Locate every blood parasite and identify its species.
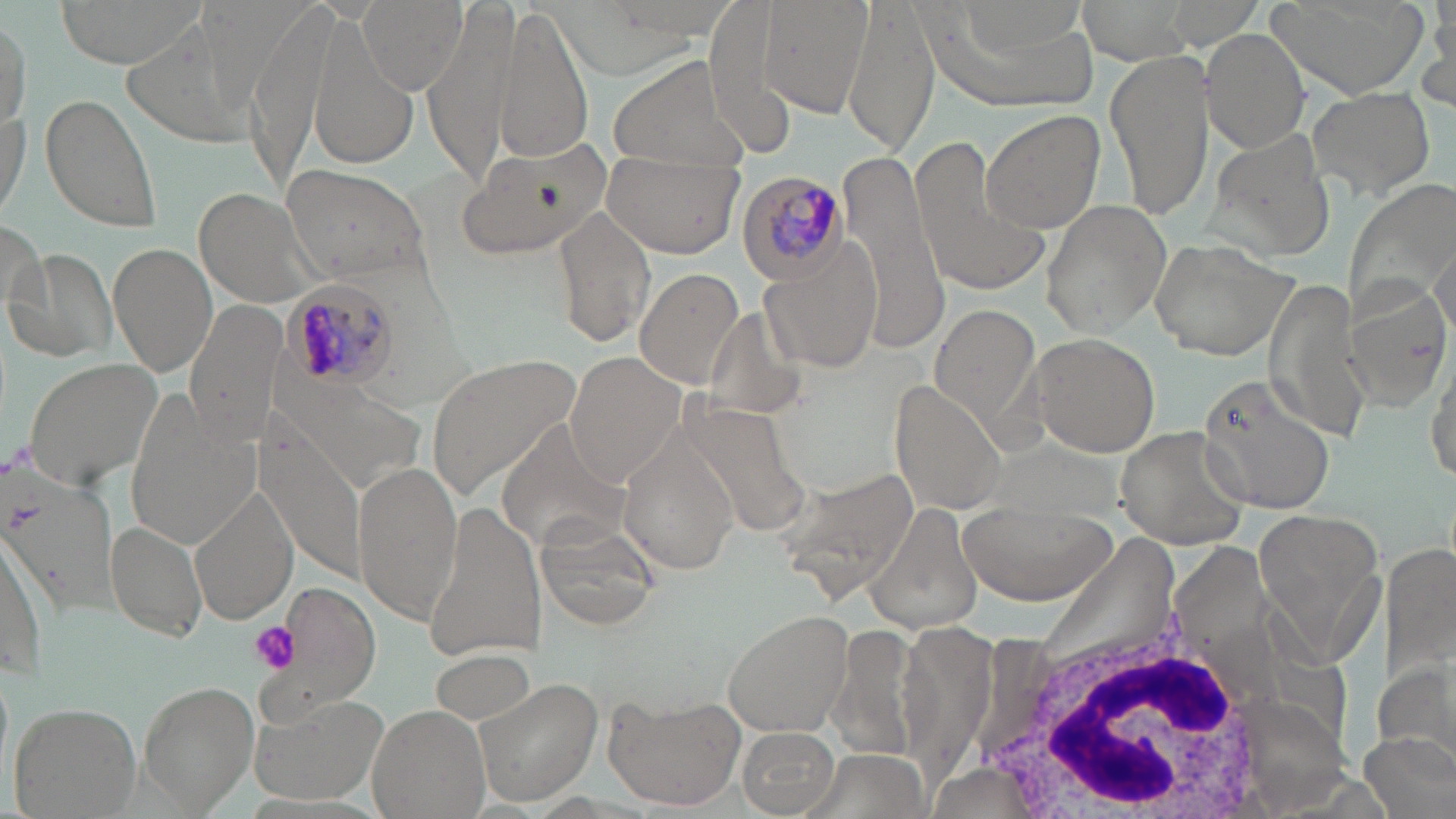

Approximate bounding boxes as [x1, y1, x2, y2] in pixels.
Plasmodium malariae-infected red blood cells: [736, 171, 849, 284], [280, 278, 398, 390].
No Plasmodium falciparum, Plasmodium ovale, Plasmodium vivax, Babesia divergens, or Trypanosoma brucei observed.

Summary:
  - Uninfected red blood cell locations: [52, 0, 205, 67], [247, 0, 341, 193], [358, 0, 465, 94], [756, 0, 874, 116], [844, 0, 938, 154], [1164, 0, 1267, 49], [1263, 0, 1429, 103], [1077, 1, 1197, 65], [425, 2, 516, 183], [1426, 3, 1455, 101], [1, 7, 31, 139], [491, 7, 594, 169], [304, 16, 418, 177], [1202, 28, 1309, 153], [1104, 50, 1215, 221], [606, 53, 750, 176], [1305, 84, 1436, 202], [41, 92, 164, 233], [0, 101, 31, 224], [979, 109, 1104, 233], [1207, 131, 1339, 261], [457, 137, 612, 262], [908, 139, 1052, 300], [841, 146, 951, 335], [600, 153, 744, 260], [278, 162, 433, 284], [1345, 177, 1456, 318], [193, 188, 327, 309], [1039, 200, 1172, 338], [549, 203, 658, 352], [1, 215, 53, 328], [1147, 238, 1298, 361], [759, 240, 884, 377], [109, 241, 217, 378], [1430, 242, 1455, 335], [5, 248, 118, 363], [633, 266, 747, 390], [1263, 281, 1376, 444], [1340, 283, 1450, 414], [183, 297, 284, 443], [928, 301, 1043, 438], [1029, 333, 1161, 458], [425, 351, 585, 498], [566, 352, 686, 482], [1426, 354, 1456, 485], [23, 357, 161, 489], [1198, 372, 1334, 517], [890, 379, 1007, 516], [128, 401, 259, 544], [496, 422, 628, 557], [1116, 423, 1251, 549], [617, 435, 742, 575], [354, 462, 465, 622], [779, 466, 920, 601], [3, 468, 117, 612], [191, 483, 299, 624], [421, 498, 546, 663], [868, 502, 985, 636], [955, 502, 1114, 607], [1254, 506, 1387, 651], [529, 516, 663, 633], [105, 518, 209, 644], [0, 535, 50, 681], [1382, 537, 1456, 696], [262, 579, 382, 723], [721, 609, 855, 734], [830, 622, 926, 766], [428, 644, 541, 729], [1377, 656, 1456, 768], [473, 677, 604, 807], [138, 682, 260, 812], [603, 692, 746, 811], [249, 695, 388, 805], [8, 701, 141, 819], [368, 704, 489, 819], [735, 723, 843, 817], [1359, 731, 1454, 819], [801, 751, 926, 819]
  - White blood cell locations: [971, 603, 1281, 819]
  - Platelet locations: [248, 620, 300, 675]
  - Slide-level diagnosis: Plasmodium malariae
  - Field of view: single
  - Magnification: 1000x
  - Stain: May-Grünwald-Giemsa
  - Modality: optical microscopy
  - Preparation: thin blood film
  - Image size: 1456×819 pixels